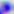
identification = Toxoplasma gondii
magnification = 400x
modality = photomicrograph